Give the extent of all uninfected red blood cells.
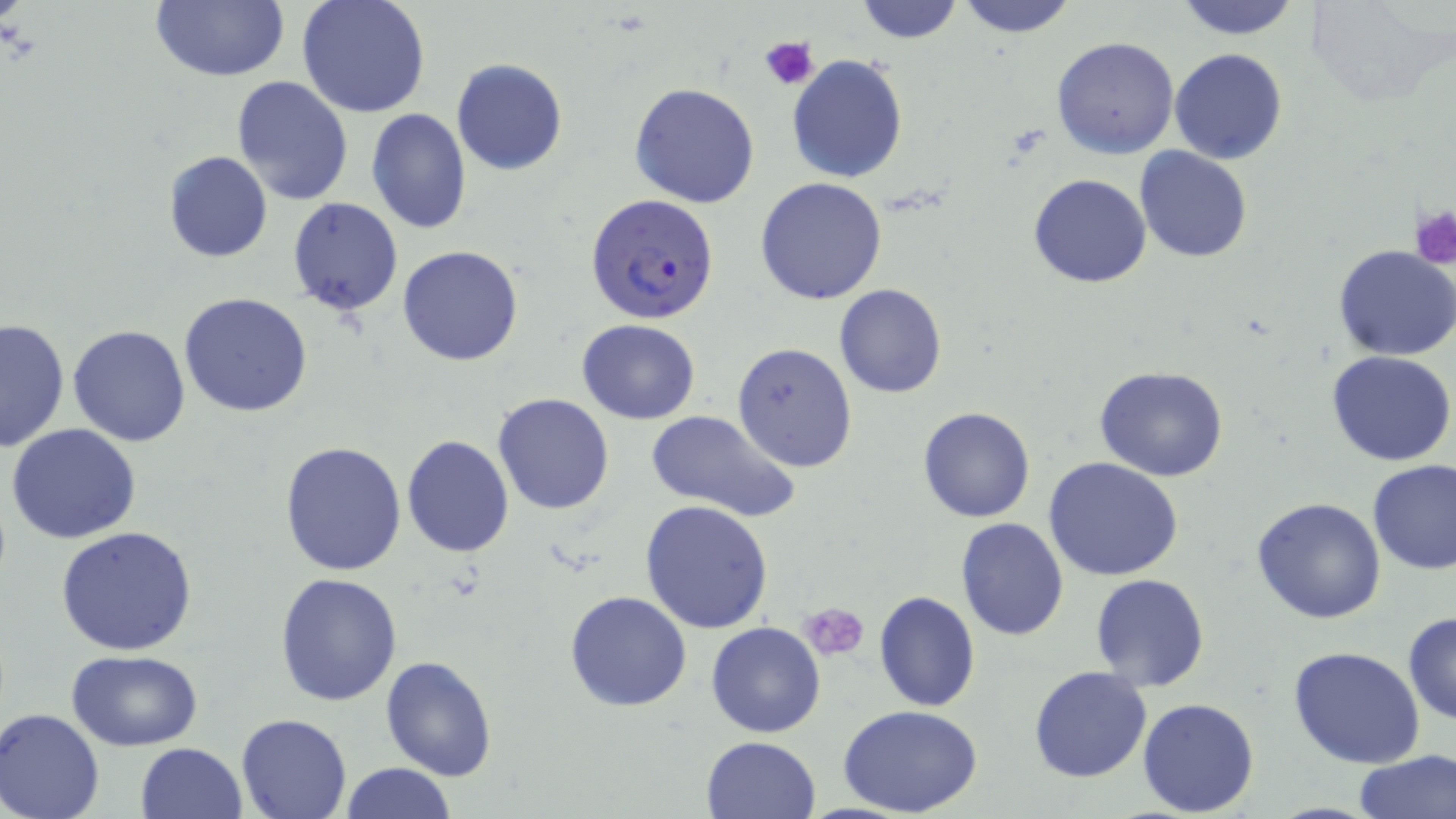
Approximate bounding boxes as named x1/y1/x2/y2 corners in pixels.
Uninfected red blood cells: (x1=151, y1=0, x2=290, y2=81), (x1=296, y1=0, x2=430, y2=120), (x1=855, y1=0, x2=965, y2=44), (x1=1172, y1=0, x2=1303, y2=40), (x1=1304, y1=0, x2=1446, y2=105), (x1=955, y1=1, x2=1079, y2=38), (x1=1052, y1=36, x2=1179, y2=158), (x1=1170, y1=47, x2=1289, y2=165), (x1=786, y1=54, x2=909, y2=183), (x1=451, y1=57, x2=568, y2=177), (x1=230, y1=75, x2=354, y2=205), (x1=629, y1=82, x2=761, y2=208), (x1=365, y1=107, x2=472, y2=235), (x1=1135, y1=146, x2=1254, y2=263), (x1=164, y1=150, x2=272, y2=262), (x1=1026, y1=159, x2=1252, y2=272), (x1=1027, y1=174, x2=1153, y2=289), (x1=756, y1=176, x2=888, y2=304), (x1=287, y1=196, x2=404, y2=317), (x1=398, y1=245, x2=523, y2=367), (x1=1333, y1=245, x2=1456, y2=362), (x1=834, y1=283, x2=948, y2=399), (x1=179, y1=292, x2=313, y2=417), (x1=70, y1=310, x2=309, y2=433), (x1=0, y1=317, x2=69, y2=453), (x1=576, y1=319, x2=701, y2=425), (x1=68, y1=323, x2=193, y2=447), (x1=732, y1=341, x2=857, y2=470), (x1=1327, y1=350, x2=1456, y2=466), (x1=1094, y1=366, x2=1229, y2=482), (x1=492, y1=392, x2=616, y2=515), (x1=917, y1=406, x2=1036, y2=523), (x1=644, y1=410, x2=803, y2=524), (x1=6, y1=421, x2=141, y2=543), (x1=401, y1=434, x2=516, y2=557), (x1=279, y1=440, x2=408, y2=578), (x1=1043, y1=456, x2=1185, y2=581), (x1=1366, y1=459, x2=1456, y2=577), (x1=1249, y1=497, x2=1389, y2=625), (x1=640, y1=499, x2=773, y2=632), (x1=955, y1=518, x2=1070, y2=640), (x1=55, y1=526, x2=197, y2=655), (x1=275, y1=571, x2=402, y2=705), (x1=1089, y1=573, x2=1210, y2=692), (x1=873, y1=590, x2=981, y2=712), (x1=565, y1=591, x2=693, y2=712), (x1=1403, y1=611, x2=1455, y2=725), (x1=706, y1=621, x2=827, y2=738), (x1=1286, y1=645, x2=1429, y2=769), (x1=66, y1=649, x2=203, y2=748), (x1=380, y1=656, x2=498, y2=781), (x1=1028, y1=666, x2=1153, y2=783), (x1=1135, y1=697, x2=1260, y2=816), (x1=838, y1=705, x2=986, y2=818), (x1=1, y1=708, x2=105, y2=819), (x1=236, y1=713, x2=352, y2=819), (x1=699, y1=736, x2=822, y2=819), (x1=135, y1=742, x2=249, y2=819), (x1=1354, y1=750, x2=1456, y2=819), (x1=339, y1=763, x2=457, y2=819).

slide-level diagnosis = Plasmodium falciparum
stain = May-Grünwald-Giemsa
modality = light microscopy
field of view = single
preparation = thin blood film
image size = 1456×819 pixels
Plasmodium falciparum-infected red blood cell locations = approximate bounding boxes as named x1/y1/x2/y2 corners in pixels: (x1=584, y1=193, x2=719, y2=326)
platelet locations = approximate bounding boxes as named x1/y1/x2/y2 corners in pixels: (x1=758, y1=35, x2=818, y2=91), (x1=1408, y1=203, x2=1456, y2=267), (x1=802, y1=602, x2=870, y2=661)
magnification = 1000x